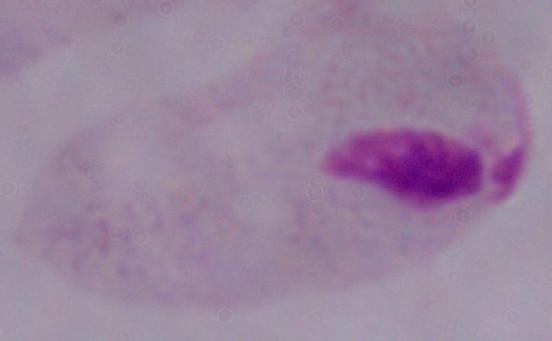
A trichomonad is seen. 1000x magnification. Photomicrograph.